State which parasite is depicted.
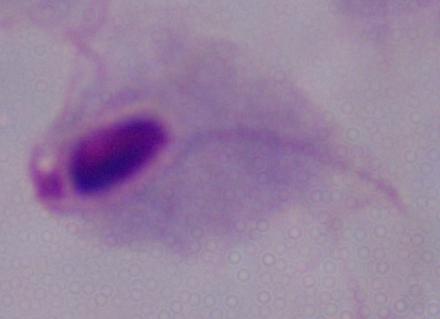

A trichomonad.

{
  "modality": "micrograph",
  "magnification": "1000x"
}